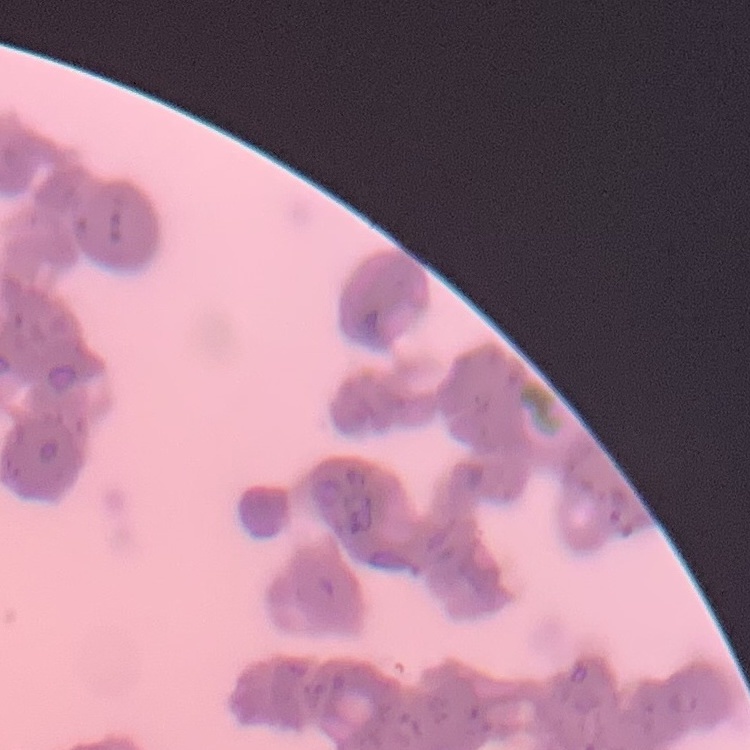
The erythrocytes exhibit rouleaux formation. Thin blood film. Stained with either Field's or Giemsa. One tile cut from a larger photomicrograph.